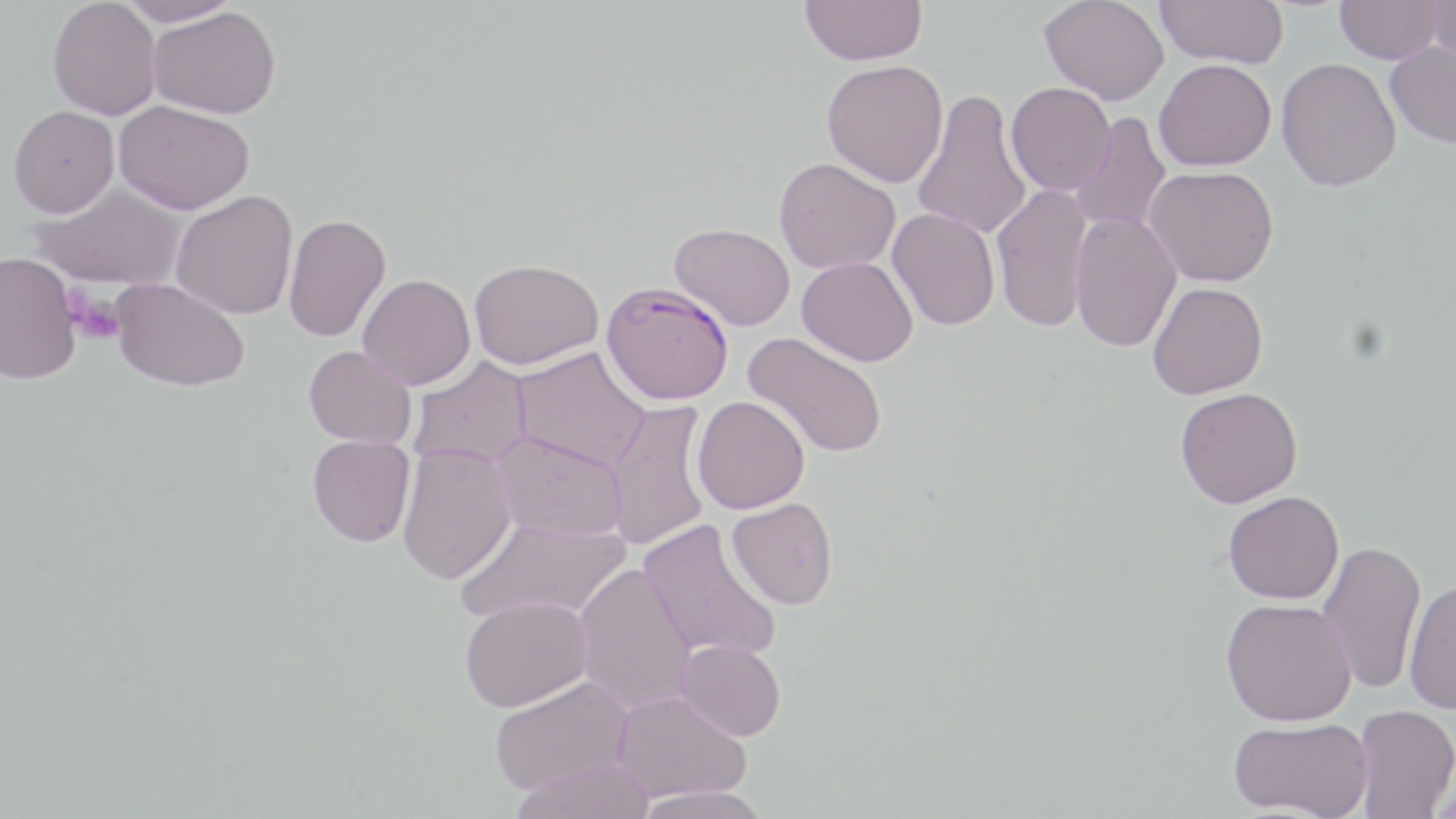

Summary:
  - Coordinate format: approximate bounding boxes as [x1, y1, x2, y2] in pixels
  - Uninfected red blood cell locations: [47, 0, 161, 120], [116, 0, 242, 27], [800, 0, 927, 66], [1039, 0, 1169, 105], [1156, 0, 1289, 68], [1335, 0, 1444, 64], [1429, 0, 1456, 71], [148, 6, 280, 118], [1385, 41, 1456, 148], [1276, 57, 1401, 192], [1153, 58, 1276, 171], [821, 59, 948, 187], [1005, 83, 1115, 196], [912, 89, 1032, 241], [114, 100, 254, 215], [8, 105, 119, 217], [1069, 112, 1171, 234], [774, 157, 901, 274], [1144, 166, 1279, 287], [30, 184, 187, 290], [991, 184, 1095, 333], [171, 190, 298, 319], [887, 207, 1000, 330], [1070, 210, 1182, 353], [283, 214, 391, 343], [669, 222, 795, 330], [0, 251, 81, 384], [797, 256, 918, 366], [469, 258, 603, 370], [358, 273, 475, 390], [111, 277, 250, 392], [1147, 282, 1267, 400], [742, 331, 889, 459], [303, 345, 417, 448], [510, 346, 651, 471], [408, 356, 533, 469], [1175, 387, 1302, 508], [692, 396, 810, 514], [604, 399, 712, 552], [492, 430, 628, 541], [307, 435, 416, 547], [397, 444, 517, 585], [1223, 490, 1344, 604], [727, 497, 838, 609], [456, 517, 630, 626], [638, 518, 782, 662], [1317, 540, 1426, 695], [573, 562, 697, 714], [1404, 580, 1456, 714], [459, 594, 593, 711], [1220, 598, 1356, 726], [676, 639, 786, 740], [488, 675, 634, 796], [611, 689, 751, 804], [1353, 704, 1456, 818], [1228, 717, 1373, 818], [511, 759, 655, 819], [1430, 775, 1455, 819], [632, 785, 771, 819]
  - Plasmodium falciparum-infected red blood cell locations: [600, 281, 734, 405]
  - Platelet locations: [67, 291, 127, 344]
  - Slide-level diagnosis: Plasmodium falciparum
  - Image size: 1456×819 pixels
  - Field of view: one of a larger specimen
  - Modality: optical microscopy
  - Stain: May-Grünwald-Giemsa
  - Magnification: 1000x
  - Preparation: thin blood smear